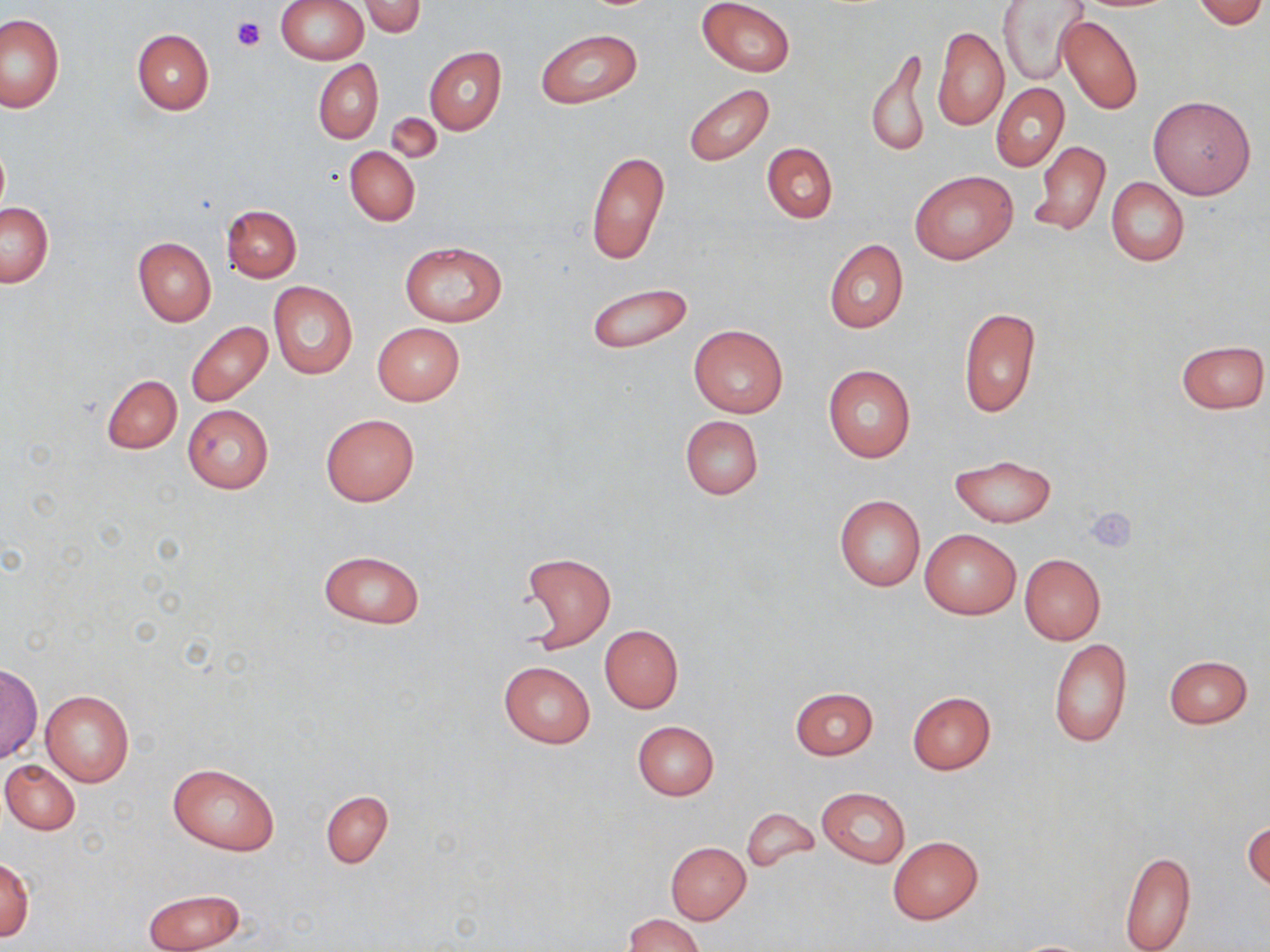

slide-level diagnosis = no evidence of blood parasites
stain = May-Grünwald-Giemsa
uninfected red blood cell locations = approximate bounding boxes as [x1, y1, x2, y2] in pixels: [276, 0, 368, 64], [697, 0, 796, 76], [1191, 0, 1267, 28], [360, 1, 425, 37], [996, 1, 1088, 86], [0, 15, 65, 114], [1057, 15, 1143, 115], [933, 27, 1008, 132], [131, 28, 214, 116], [535, 28, 643, 108], [865, 45, 930, 160], [424, 47, 505, 134], [314, 59, 382, 143], [683, 83, 775, 166], [991, 83, 1069, 172], [1148, 96, 1255, 199], [385, 114, 441, 165], [1029, 140, 1111, 235], [762, 142, 837, 224], [345, 147, 420, 226], [585, 150, 670, 268], [910, 170, 1015, 265], [1106, 178, 1189, 266], [1, 203, 54, 287], [222, 204, 301, 282], [132, 237, 216, 326], [824, 239, 908, 333], [399, 241, 507, 325], [268, 281, 358, 380], [586, 281, 693, 354], [958, 307, 1041, 418], [185, 321, 273, 407], [372, 322, 464, 406], [687, 323, 789, 417], [1176, 340, 1269, 414], [823, 364, 916, 461], [102, 374, 182, 453], [182, 404, 273, 494], [320, 414, 419, 507], [679, 415, 762, 501], [951, 455, 1056, 527], [834, 494, 925, 592], [920, 529, 1020, 620], [317, 550, 425, 628], [518, 552, 616, 652], [1019, 554, 1105, 644], [600, 625, 683, 713], [1049, 638, 1131, 747], [1164, 656, 1253, 729], [498, 660, 596, 748], [1, 662, 41, 764], [790, 687, 877, 759], [40, 689, 135, 787], [907, 692, 996, 774], [632, 720, 719, 800], [1, 759, 80, 835], [167, 762, 280, 855], [817, 786, 909, 868], [320, 789, 393, 868], [742, 807, 817, 873], [1244, 820, 1270, 890], [888, 836, 982, 924], [666, 842, 751, 924], [1119, 850, 1196, 952], [0, 858, 34, 941], [143, 888, 246, 952], [624, 914, 705, 952], [1009, 939, 1099, 951]
field of view = one of a larger specimen
magnification = 1000x
image size = 1270×952 pixels
platelet locations = approximate bounding boxes as [x1, y1, x2, y2] in pixels: [233, 16, 265, 51], [1084, 506, 1138, 553]
modality = optical microscopy
preparation = thin blood smear